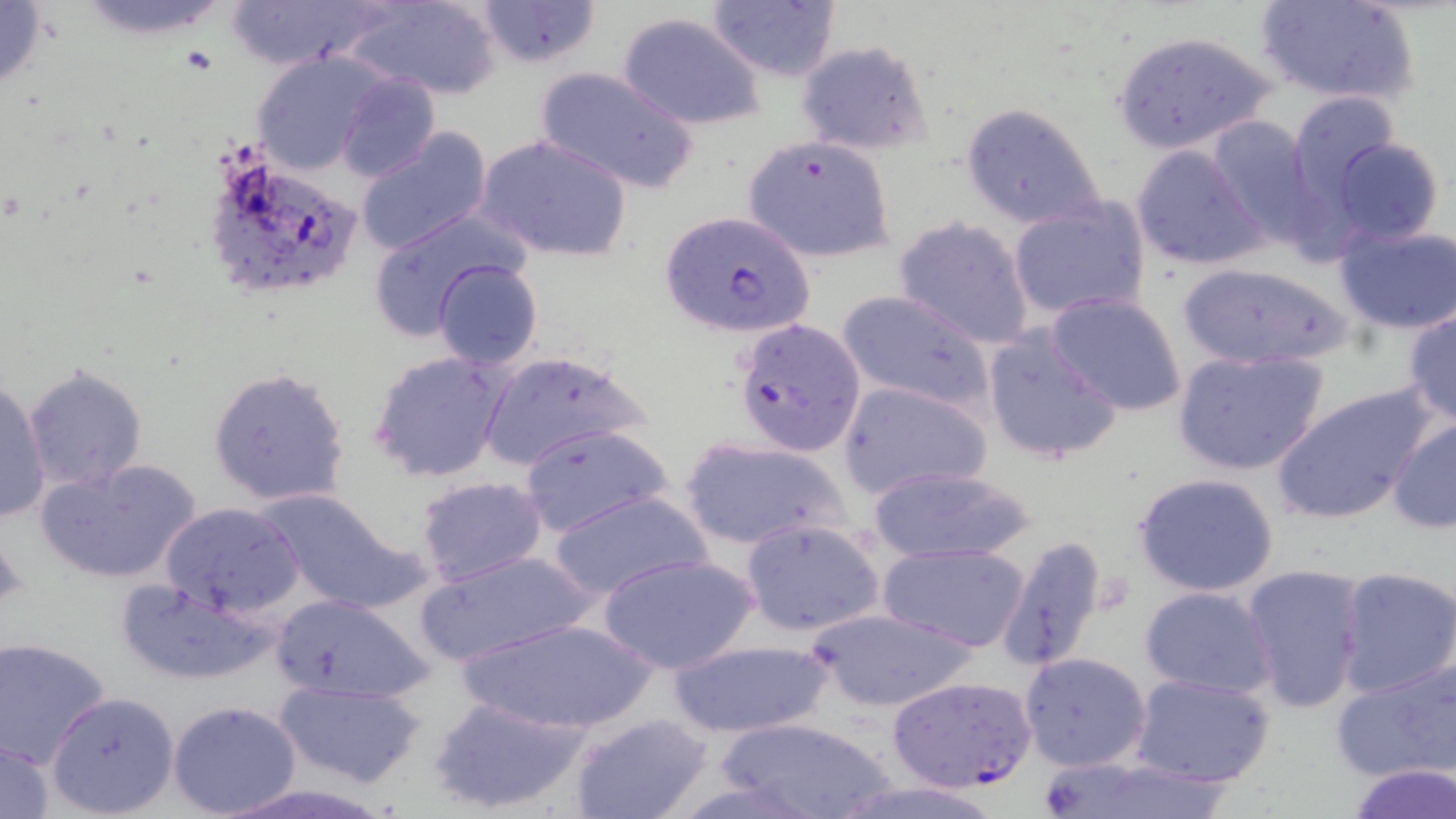

Summary:
  - Coordinate format: approximate bounding boxes as (x1, y1, x2, y2) in pixels
  - Uninfected red blood cell locations: (0, 0, 51, 97), (225, 0, 381, 70), (343, 0, 502, 101), (474, 0, 602, 69), (1253, 0, 1419, 107), (706, 2, 841, 81), (616, 11, 769, 130), (1109, 29, 1277, 155), (793, 39, 933, 157), (247, 51, 388, 175), (533, 66, 699, 196), (335, 74, 440, 181), (1286, 91, 1400, 214), (958, 102, 1106, 232), (1203, 116, 1320, 248), (356, 128, 493, 255), (476, 134, 633, 264), (741, 136, 896, 265), (1330, 136, 1445, 245), (1131, 143, 1270, 272), (1007, 199, 1153, 323), (366, 210, 532, 343), (893, 216, 1036, 350), (1332, 218, 1456, 337), (432, 260, 543, 370), (1172, 262, 1360, 370), (837, 289, 995, 416), (1045, 292, 1187, 417), (1402, 307, 1456, 426), (981, 326, 1125, 467), (1171, 347, 1330, 477), (367, 349, 515, 484), (478, 349, 650, 472), (23, 365, 148, 494), (206, 366, 351, 508), (0, 376, 50, 524), (838, 379, 992, 500), (1271, 381, 1441, 526), (1385, 415, 1456, 533), (519, 423, 674, 539), (677, 436, 852, 552), (34, 458, 203, 586), (863, 465, 1042, 565), (1131, 472, 1282, 598), (414, 476, 548, 588), (257, 488, 428, 616), (550, 490, 710, 603), (160, 501, 304, 618), (739, 519, 887, 638), (993, 534, 1111, 674), (880, 542, 1031, 653), (417, 548, 597, 666), (598, 553, 757, 676), (1239, 563, 1367, 715), (1336, 566, 1456, 698), (114, 579, 275, 687), (1138, 585, 1281, 698), (267, 594, 436, 703), (807, 607, 983, 713), (458, 616, 657, 735), (1, 636, 113, 767), (663, 640, 837, 740), (1018, 651, 1152, 773), (1331, 655, 1456, 783), (1129, 671, 1279, 788), (272, 678, 427, 787), (47, 690, 179, 816), (426, 694, 599, 817), (168, 700, 303, 818), (567, 713, 714, 819), (710, 715, 902, 819), (1, 735, 56, 818), (1033, 754, 1238, 819), (1344, 763, 1456, 819), (829, 779, 1010, 819)
  - Plasmodium falciparum-infected red blood cell locations: (199, 144, 367, 305), (659, 211, 817, 340), (733, 317, 866, 457), (885, 674, 1039, 793)
  - Slide-level diagnosis: Plasmodium falciparum
  - Preparation: thin blood smear
  - Field of view: one of a larger specimen
  - Magnification: 1000x
  - Modality: optical microscopy
  - Stain: May-Grünwald-Giemsa
  - Image size: 1456×819 pixels